Locate every blood parasite and identify its species.
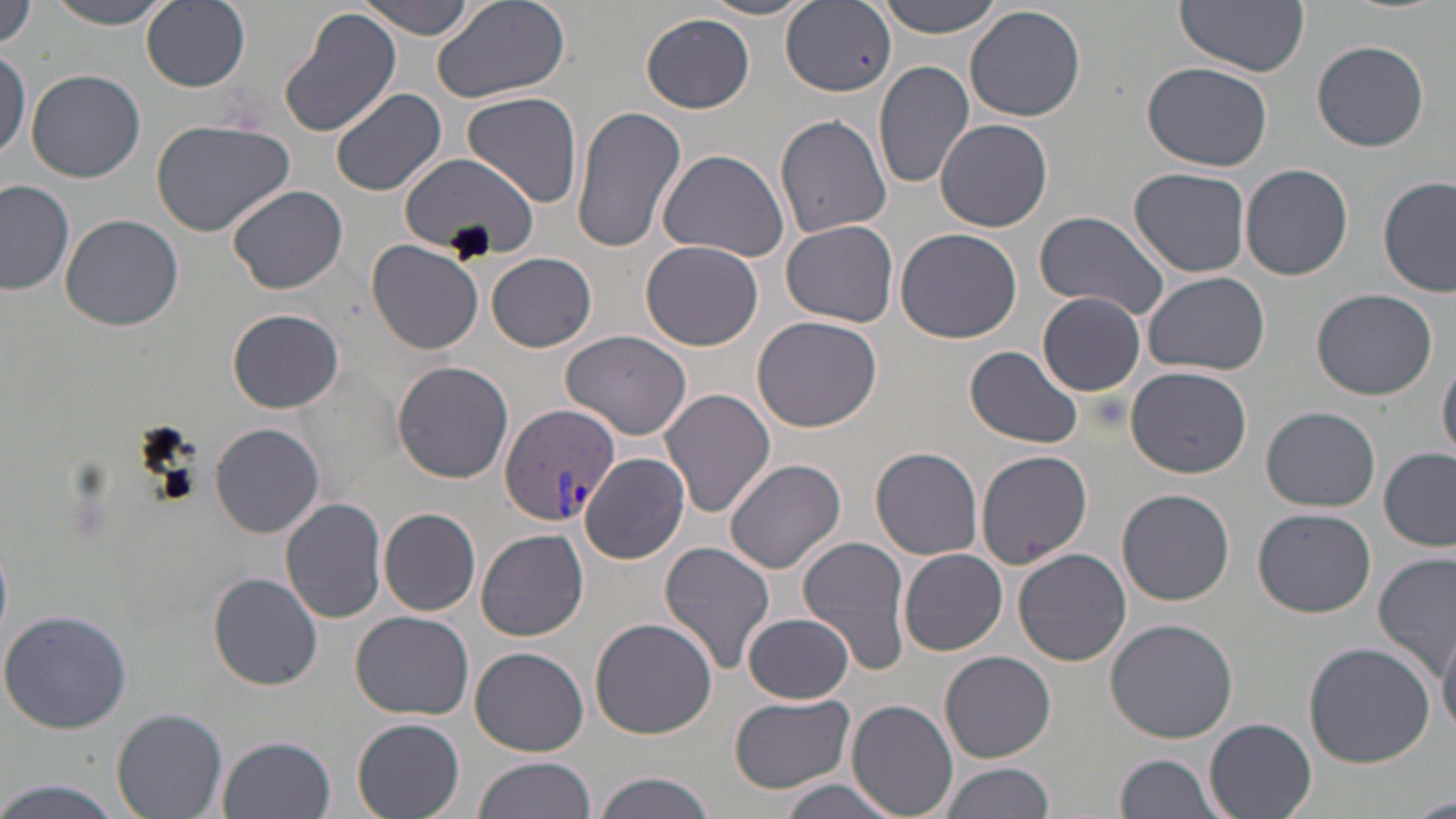
Approximate bounding boxes as (x1,y1)-(x2,y2) corner pairs in pixels.
Plasmodium vivax-infected red blood cells: (498,403)-(621,528).
No Plasmodium falciparum, Plasmodium ovale, Plasmodium malariae, Babesia divergens, or Trypanosoma brucei observed.

slide_level_diagnosis: Plasmodium vivax
preparation: thin blood film
magnification: 1000x
stain: May-Grünwald-Giemsa
field_of_view: one of a larger specimen
modality: optical microscopy
uninfected_red_blood_cell_locations: 'approximate bounding boxes as (x1,y1)-(x2,y2) corner pairs in pixels: (43,0)-(180,28), (142,0)-(250,91), (430,0)-(573,105), (875,0)-(1006,37), (1176,0)-(1312,74), (355,1)-(480,40), (697,1)-(818,20), (0,3)-(34,51), (780,3)-(898,97), (276,4)-(402,139), (964,5)-(1087,122), (641,13)-(755,113), (1314,40)-(1429,151), (438,45)-(581,176), (0,50)-(29,165), (874,61)-(974,190), (1141,62)-(1273,172), (25,68)-(146,183), (331,87)-(446,198), (462,92)-(583,209), (567,104)-(686,255), (775,114)-(892,239), (936,119)-(1053,232), (150,120)-(293,237), (657,147)-(789,260), (397,151)-(536,259), (1240,164)-(1355,280), (1128,166)-(1252,277), (1378,177)-(1454,297), (1,179)-(75,296), (227,185)-(348,295), (1031,209)-(1172,320), (62,214)-(183,330), (779,220)-(899,326), (895,229)-(1024,344), (366,239)-(485,354), (641,240)-(765,349), (487,253)-(597,352), (1142,271)-(1270,377), (1312,288)-(1438,400), (1037,292)-(1147,396), (229,308)-(342,413), (753,316)-(882,430), (561,330)-(694,440), (965,346)-(1084,450), (1438,358)-(1456,465), (391,360)-(514,482), (1127,365)-(1252,477), (659,389)-(776,518), (1261,406)-(1381,511), (209,423)-(325,537), (870,446)-(984,560), (974,447)-(1094,570), (1380,447)-(1455,552), (580,452)-(690,564), (724,458)-(847,575), (1116,487)-(1236,605), (280,498)-(389,623), (1253,507)-(1377,619), (379,508)-(481,615), (476,528)-(590,641), (792,532)-(917,672), (659,539)-(776,676), (1013,548)-(1131,666), (898,549)-(1007,655), (1374,551)-(1454,680), (209,573)-(323,690), (0,609)-(132,734), (349,610)-(475,719), (745,610)-(851,704), (589,616)-(717,739), (1104,618)-(1239,742), (1438,629)-(1456,737), (1303,641)-(1435,768), (470,648)-(589,755), (939,650)-(1056,763), (729,694)-(856,794), (848,700)-(958,819), (112,707)-(228,818), (352,717)-(466,819), (1205,717)-(1318,818), (219,735)-(335,819), (1114,753)-(1227,819), (475,756)-(598,819), (937,761)-(1053,819), (593,773)-(717,819), (1,780)-(123,819), (777,780)-(903,819), (1407,793)-(1456,819)'
image_size: 1456×819 pixels